Report the malaria status of this cell.
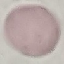

Uninfected.

Summary:
  - Preparation: thin smear
  - Stain: Giemsa
  - Image type: cell patch, automatically extracted from a larger field of view and resized to 64 × 64 pixels
  - Capture: smartphone camera at the microscope eyepiece